Comment on the morphology of the erythrocytes.
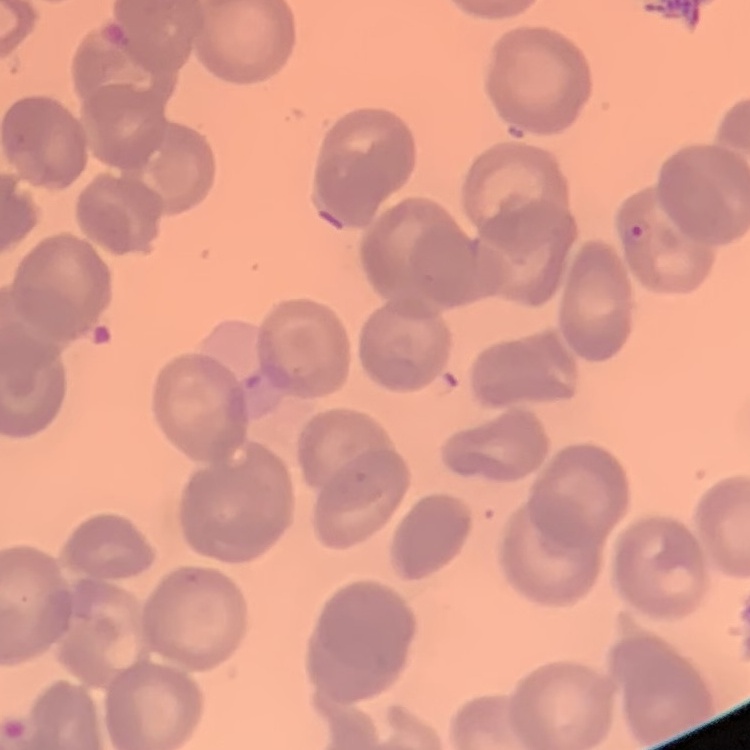

No rouleaux formation.

Thin peripheral smear. Stained with either Field's or Giemsa. Square crop of a larger photomicrograph.